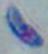

{
  "magnification": "1000x",
  "modality": "micrograph",
  "identification": "Toxoplasma gondii"
}